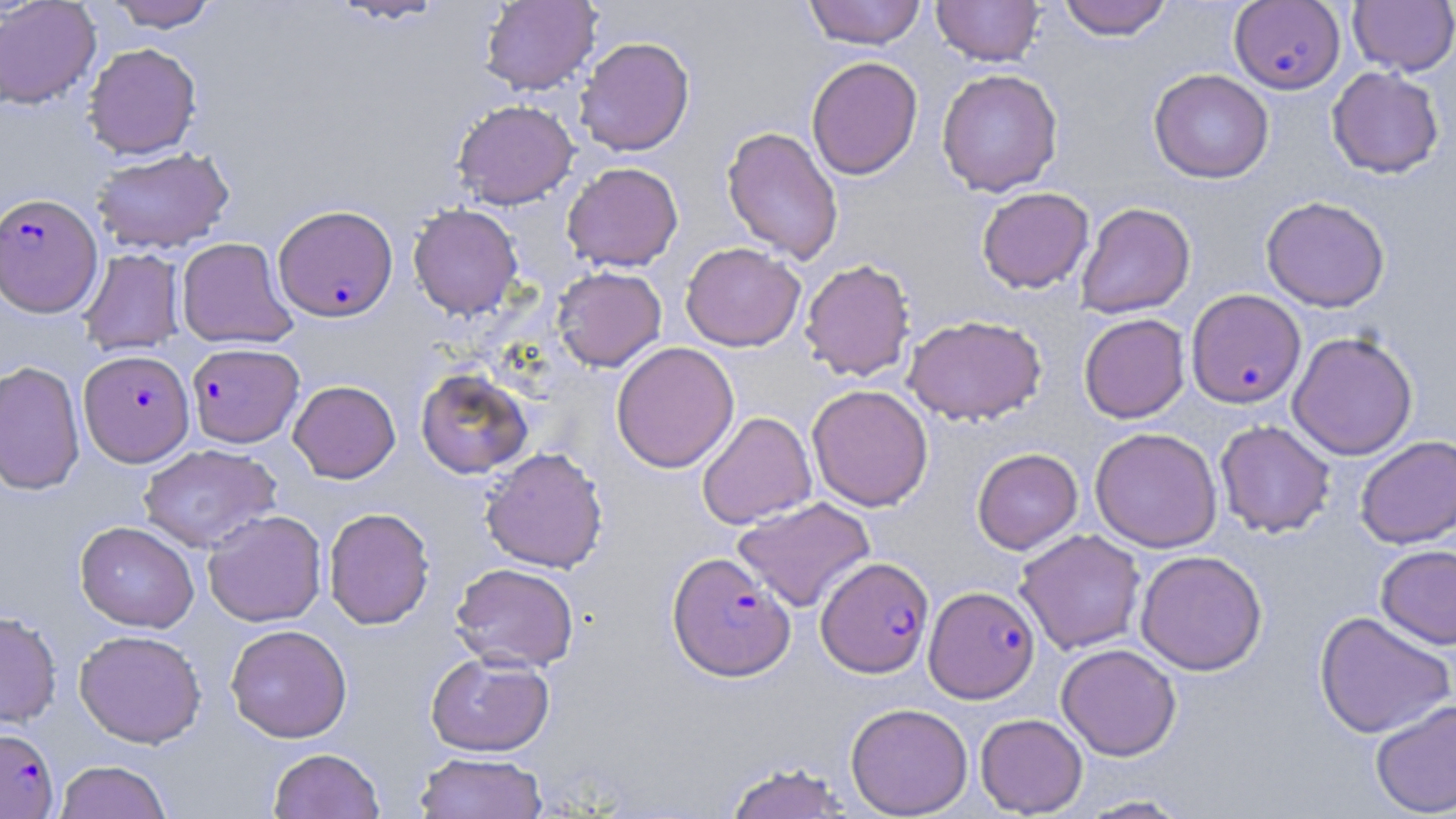
slide-level diagnosis = Plasmodium falciparum
preparation = thin blood film
field of view = single
uninfected red blood cell locations = approximate bounding boxes as (x1, y1, x2, y2) in pixels: (0, 0, 101, 110), (329, 0, 448, 25), (479, 0, 601, 95), (803, 0, 927, 49), (1057, 0, 1174, 41), (105, 1, 220, 32), (931, 1, 1044, 66), (1348, 1, 1456, 75), (575, 36, 695, 156), (82, 42, 202, 160), (806, 56, 923, 180), (1326, 66, 1444, 178), (936, 68, 1063, 196), (1148, 68, 1274, 184), (452, 99, 579, 209), (721, 126, 844, 264), (91, 147, 234, 254), (562, 162, 683, 272), (976, 187, 1094, 293), (1261, 196, 1390, 312), (1075, 202, 1196, 318), (408, 203, 523, 320), (176, 237, 298, 350), (680, 242, 805, 351), (79, 248, 185, 356), (799, 258, 916, 382), (552, 266, 667, 372), (1078, 313, 1190, 423), (904, 314, 1048, 425), (1287, 331, 1418, 459), (611, 341, 739, 473), (0, 360, 85, 496), (415, 368, 533, 479), (288, 380, 401, 483), (807, 384, 933, 512), (697, 411, 816, 529), (1215, 419, 1335, 538), (1090, 427, 1222, 553), (1356, 435, 1456, 548), (138, 444, 281, 552), (480, 446, 608, 573), (972, 448, 1083, 554), (733, 496, 876, 613), (323, 507, 435, 629), (202, 509, 327, 627), (75, 521, 200, 632), (1015, 529, 1146, 655), (1375, 544, 1456, 650), (1135, 549, 1267, 676), (450, 562, 580, 672), (0, 611, 62, 728), (1314, 611, 1455, 739), (225, 624, 352, 743), (74, 629, 207, 748), (1056, 643, 1182, 760), (425, 651, 554, 756), (1369, 699, 1456, 817), (845, 702, 973, 818), (975, 713, 1088, 817), (268, 747, 385, 819), (414, 751, 548, 818), (54, 760, 173, 819), (723, 762, 855, 818), (1075, 794, 1195, 818)
stain = May-Grünwald-Giemsa
Plasmodium falciparum-infected red blood cell locations = approximate bounding boxes as (x1, y1, x2, y2) in pixels: (1229, 2, 1345, 95), (0, 192, 103, 317), (273, 204, 398, 322), (1187, 289, 1305, 408), (186, 342, 304, 448), (79, 349, 194, 467), (667, 551, 795, 681), (816, 556, 933, 677), (924, 585, 1039, 702), (0, 727, 59, 818)
magnification = 1000x
modality = optical microscopy
image size = 1456×819 pixels